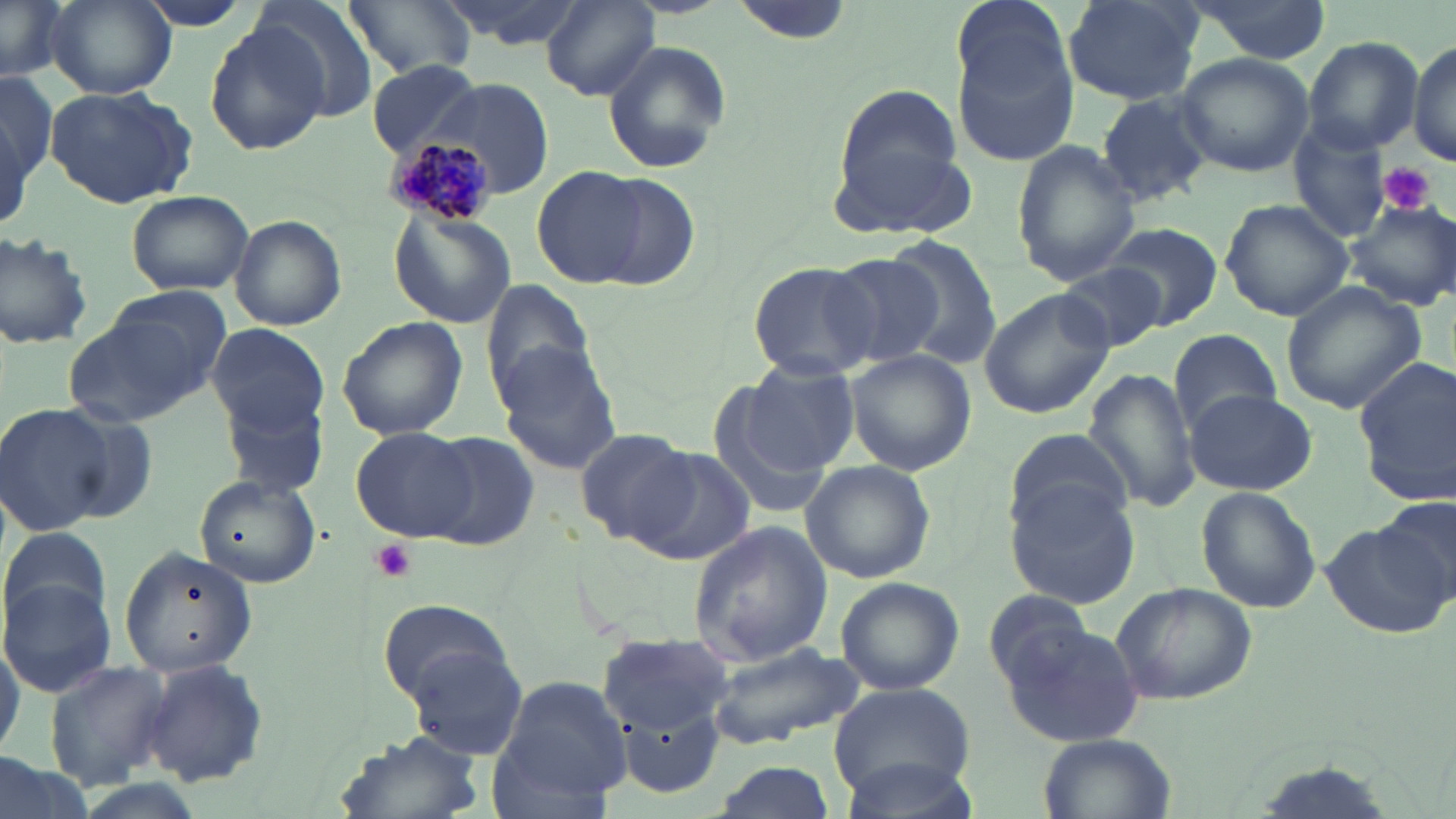

slide-level diagnosis = Plasmodium malariae
uninfected red blood cell locations = approximate bounding boxes as (x1, y1, x2, y2) in pixels: (0, 0, 68, 82), (44, 0, 175, 100), (129, 0, 264, 32), (436, 0, 589, 49), (952, 0, 1076, 103), (1062, 0, 1203, 106), (1186, 0, 1331, 66), (248, 1, 381, 120), (346, 1, 471, 80), (541, 2, 660, 100), (203, 21, 329, 156), (949, 33, 1079, 168), (1302, 37, 1424, 154), (1406, 40, 1456, 167), (601, 41, 732, 176), (1174, 53, 1315, 176), (368, 61, 486, 157), (1, 71, 55, 215), (427, 77, 555, 200), (44, 82, 197, 209), (838, 83, 957, 184), (1097, 93, 1213, 206), (1287, 123, 1394, 243), (829, 140, 980, 241), (1012, 141, 1137, 289), (534, 167, 650, 288), (590, 175, 702, 291), (124, 190, 253, 296), (1219, 199, 1355, 320), (1345, 200, 1456, 308), (388, 209, 516, 330), (229, 214, 347, 330), (1102, 221, 1224, 329), (0, 231, 93, 352), (886, 237, 1005, 366), (824, 250, 946, 368), (747, 260, 879, 382), (1055, 261, 1167, 354), (482, 279, 594, 404), (1281, 281, 1428, 415), (978, 288, 1114, 419), (65, 301, 219, 428), (337, 316, 468, 441), (204, 322, 329, 436), (1167, 330, 1285, 428), (492, 344, 623, 475), (845, 350, 977, 474), (1352, 355, 1456, 509), (740, 363, 860, 473), (1083, 368, 1201, 515), (1182, 388, 1315, 495), (223, 395, 327, 496), (712, 397, 838, 520), (0, 400, 130, 539), (350, 428, 479, 541), (575, 428, 702, 547), (1009, 428, 1133, 535), (422, 432, 541, 550), (632, 446, 758, 567), (800, 460, 935, 583), (193, 474, 322, 588), (1006, 483, 1141, 608), (1196, 485, 1322, 614), (1371, 500, 1455, 614), (687, 520, 832, 667), (1, 523, 113, 640), (1320, 524, 1451, 639), (118, 546, 261, 678), (2, 576, 118, 697), (834, 576, 966, 697), (1109, 581, 1257, 706), (979, 589, 1104, 692), (375, 597, 512, 703), (998, 620, 1147, 750), (0, 622, 23, 761), (594, 632, 736, 731), (706, 638, 866, 746), (406, 644, 531, 762), (139, 658, 270, 790), (43, 659, 173, 788), (498, 675, 633, 803), (829, 683, 978, 805), (618, 706, 727, 799), (334, 731, 484, 819), (1040, 733, 1173, 818), (0, 748, 87, 819), (835, 752, 983, 819), (711, 761, 839, 819)
image size = 1456×819 pixels
magnification = 1000x
modality = optical microscopy
field of view = single
Plasmodium malariae-infected red blood cell locations = approximate bounding boxes as (x1, y1, x2, y2) in pixels: (383, 136, 493, 224)
platelet locations = approximate bounding boxes as (x1, y1, x2, y2) in pixels: (1381, 162, 1434, 214), (369, 538, 418, 582)
preparation = thin blood film
stain = May-Grünwald-Giemsa